Locate every Plasmodium parasite.
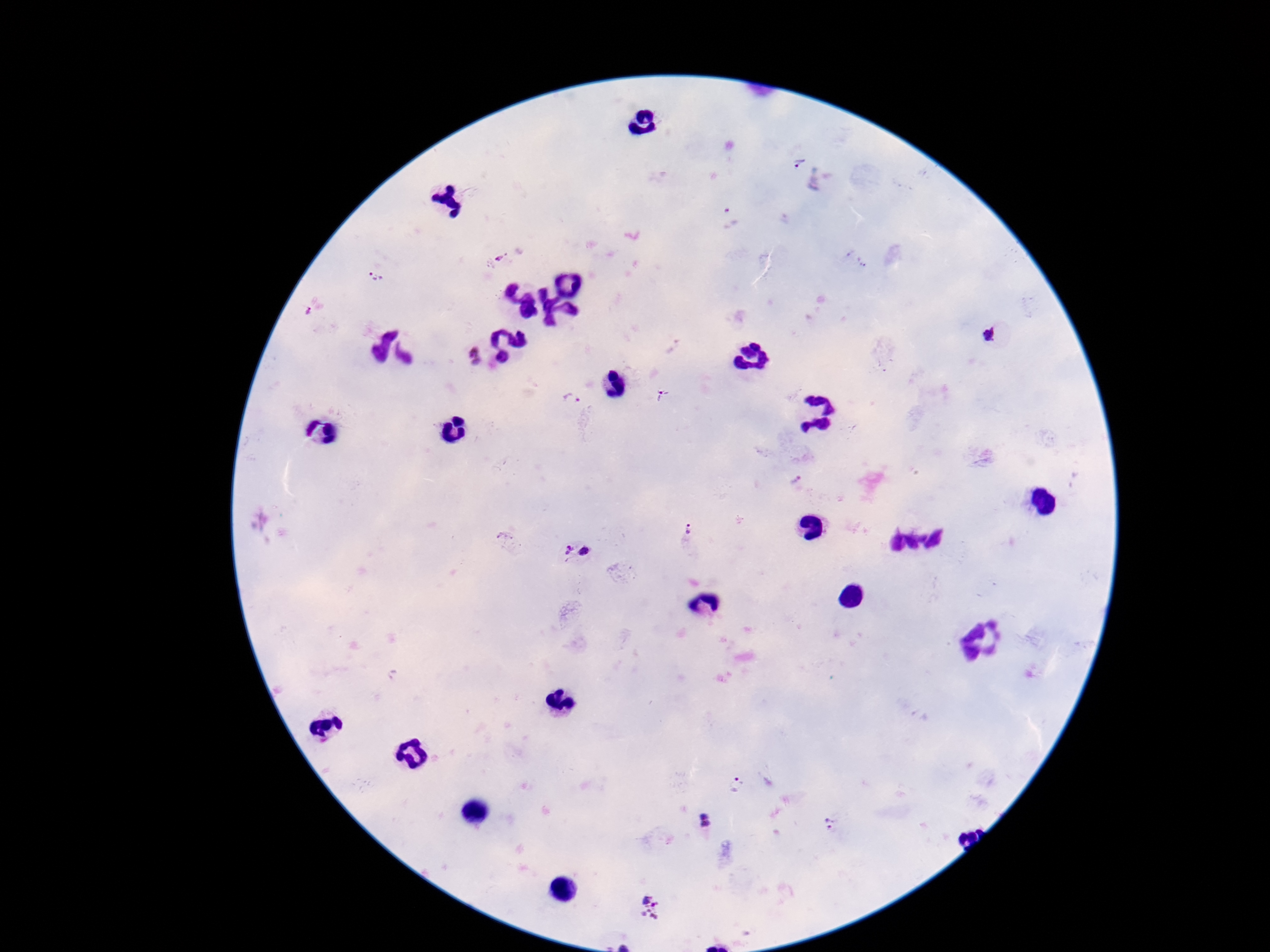

Approximate centers as {x, y} in pixels.
Plasmodium parasites: {799, 166}, {729, 217}, {499, 258}, {378, 276}, {312, 312}, {990, 336}, {473, 357}, {664, 397}, {572, 401}, {796, 481}, {688, 529}, {506, 538}, {577, 552}, {738, 785}, {706, 821}, {830, 824}, {650, 908}.

100x magnification. Image is 1270×952 pixels. Photographed through the microscope eyepiece with a smartphone camera. Patient malaria status: infected. Giemsa-stained preparation. Single field of view. Thick peripheral-blood smear.